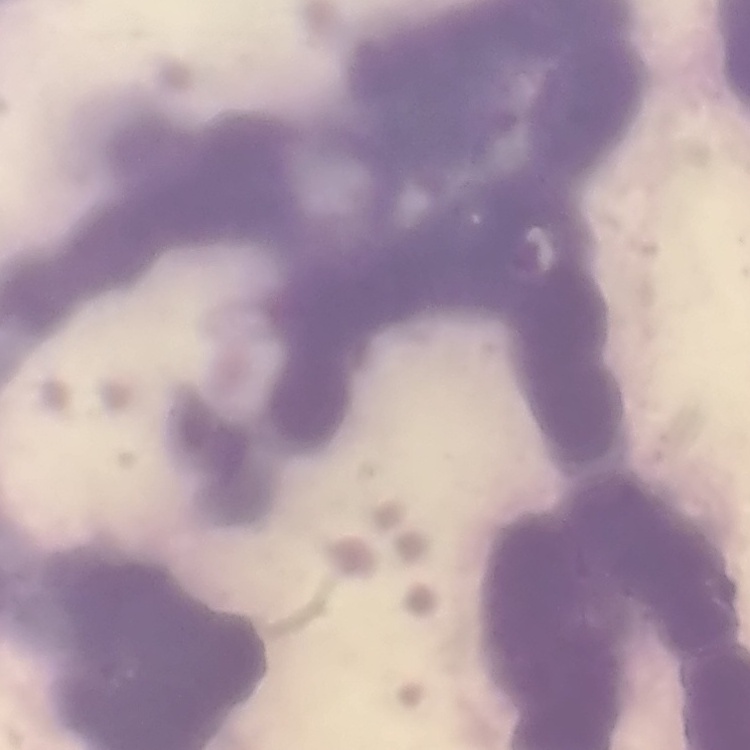 The red blood cells exhibit rouleaux formation. Stained with either Field's or Giemsa. Thin blood smear. One tile cut from a larger photomicrograph.